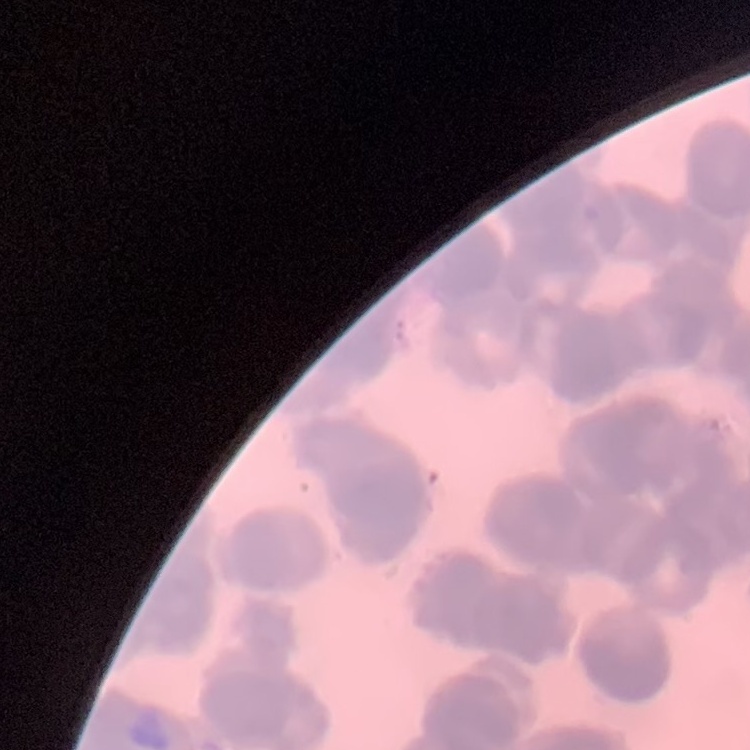

{
  "erythrocyte_morphology": "rouleaux formation",
  "preparation": "thin peripheral smear",
  "image_type": "square crop of a larger photomicrograph",
  "stain": "Field's or Giemsa"
}